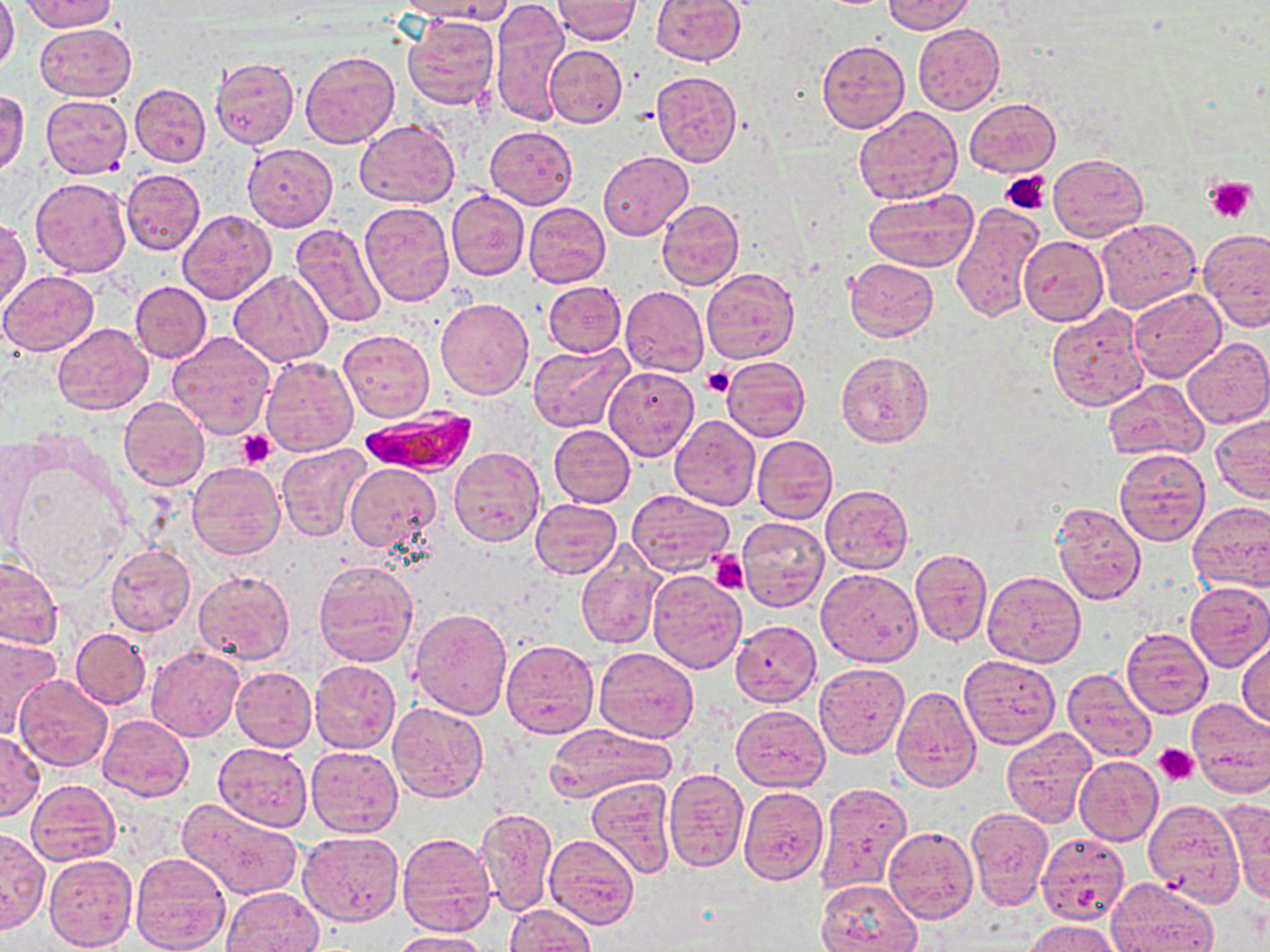
Summary:
  - Coordinate format: approximate bounding boxes as [x1, y1, x2, y2] in pixels
  - Platelet locations: [1003, 171, 1053, 214], [1206, 176, 1257, 222], [703, 367, 733, 399], [238, 430, 276, 468], [709, 551, 750, 594], [1152, 743, 1199, 785]
  - Plasmodium falciparum-infected red blood cell locations: [359, 406, 476, 478]
  - Uninfected red blood cell locations: [0, 0, 19, 72], [395, 0, 511, 23], [553, 0, 639, 43], [650, 0, 746, 65], [882, 0, 974, 34], [22, 1, 117, 32], [491, 2, 569, 127], [402, 15, 502, 110], [35, 22, 134, 100], [913, 24, 1004, 115], [817, 40, 910, 133], [543, 43, 626, 128], [299, 49, 399, 148], [209, 55, 300, 149], [650, 70, 742, 166], [130, 83, 210, 167], [1, 90, 29, 176], [40, 94, 133, 178], [964, 97, 1060, 177], [854, 106, 962, 205], [355, 120, 459, 209], [485, 126, 578, 208], [243, 143, 338, 231], [598, 151, 692, 241], [1050, 154, 1147, 240], [121, 169, 206, 254], [30, 177, 132, 277], [447, 189, 530, 280], [863, 190, 978, 273], [656, 199, 744, 290], [359, 201, 454, 306], [524, 201, 610, 287], [950, 202, 1044, 324], [178, 210, 276, 305], [1, 217, 30, 310], [1096, 218, 1201, 313], [289, 222, 387, 328], [1200, 228, 1270, 330], [1018, 235, 1108, 326], [846, 257, 937, 340], [701, 269, 799, 364], [228, 270, 332, 366], [0, 271, 100, 355], [543, 280, 625, 356], [131, 281, 211, 363], [620, 286, 708, 377], [1127, 288, 1226, 381], [436, 297, 533, 398], [1045, 305, 1150, 411], [52, 324, 153, 415], [339, 329, 434, 421], [166, 332, 275, 438], [1182, 336, 1270, 429], [528, 343, 632, 432], [835, 352, 934, 448], [259, 354, 358, 457], [721, 356, 810, 441], [603, 366, 698, 460], [1103, 378, 1207, 460], [118, 397, 209, 490], [670, 415, 760, 510], [1211, 415, 1270, 504], [550, 424, 635, 507], [752, 435, 838, 524], [0, 436, 45, 557], [276, 443, 372, 541], [449, 447, 545, 547], [1114, 447, 1212, 546], [187, 462, 284, 559], [345, 464, 439, 552], [821, 485, 913, 573], [626, 490, 733, 576], [531, 498, 622, 578], [1188, 500, 1270, 591], [1051, 502, 1146, 605], [737, 516, 829, 611], [577, 545, 663, 651], [105, 546, 195, 637], [910, 549, 991, 647], [0, 556, 61, 651], [313, 559, 420, 667], [192, 567, 296, 663], [817, 567, 922, 667], [647, 571, 746, 673], [983, 571, 1085, 667], [1184, 582, 1270, 672], [409, 607, 514, 718], [731, 621, 821, 706], [1121, 628, 1213, 718], [71, 629, 150, 707], [0, 635, 63, 739], [502, 639, 599, 738], [1237, 639, 1270, 727], [147, 646, 244, 741], [593, 647, 698, 741], [959, 656, 1060, 750], [309, 659, 400, 753], [815, 662, 909, 759], [231, 667, 316, 751], [1063, 668, 1156, 763], [14, 674, 113, 772], [890, 684, 981, 792], [1186, 698, 1270, 797], [388, 702, 488, 802], [731, 705, 829, 791], [98, 714, 195, 802], [543, 724, 675, 802], [1001, 726, 1097, 826], [0, 732, 44, 820], [213, 742, 312, 831], [306, 744, 403, 837], [1074, 755, 1163, 845], [1075, 767, 1224, 865], [663, 769, 748, 871], [588, 778, 677, 879], [25, 779, 120, 866], [816, 782, 912, 893], [739, 786, 828, 885], [179, 796, 304, 900], [1221, 797, 1269, 902], [1145, 800, 1244, 905], [477, 807, 558, 917], [965, 809, 1053, 911], [0, 827, 50, 933], [883, 827, 977, 924], [298, 830, 403, 926], [1035, 831, 1130, 925], [397, 833, 497, 937], [544, 834, 640, 929], [131, 851, 231, 952], [45, 852, 138, 951], [1108, 877, 1218, 952], [818, 879, 919, 952], [221, 887, 323, 952], [504, 904, 594, 952], [1025, 919, 1122, 952], [389, 931, 490, 951]
  - Slide-level diagnosis: Plasmodium falciparum
  - Magnification: 1000x
  - Image size: 1270×952 pixels
  - Preparation: thin blood smear
  - Stain: May-Grünwald-Giemsa
  - Modality: optical microscopy
  - Field of view: one of a larger specimen